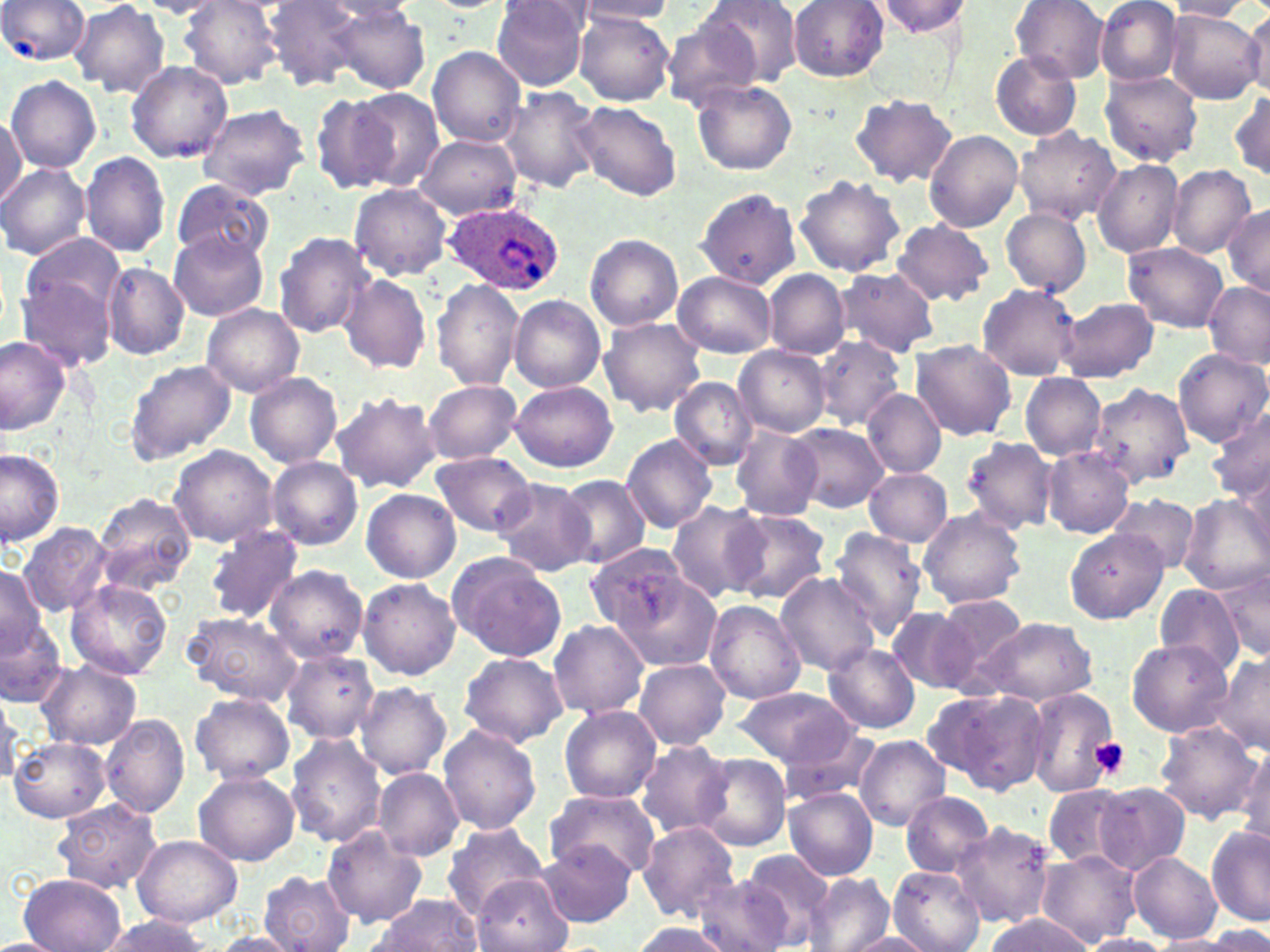

slide-level diagnosis = Plasmodium ovale
field of view = one of a larger specimen
uninfected red blood cell locations = approximate bounding boxes as named x1/y1/x2/y2 corners in pixels: (x1=0, y1=0, x2=90, y2=65), (x1=263, y1=0, x2=366, y2=89), (x1=577, y1=0, x2=679, y2=24), (x1=697, y1=0, x2=803, y2=88), (x1=1010, y1=0, x2=1110, y2=83), (x1=1095, y1=0, x2=1181, y2=85), (x1=69, y1=1, x2=169, y2=96), (x1=134, y1=1, x2=227, y2=17), (x1=178, y1=1, x2=286, y2=88), (x1=490, y1=1, x2=591, y2=90), (x1=788, y1=1, x2=889, y2=81), (x1=875, y1=1, x2=973, y2=38), (x1=1164, y1=1, x2=1252, y2=21), (x1=320, y1=2, x2=417, y2=23), (x1=331, y1=6, x2=431, y2=93), (x1=1165, y1=10, x2=1264, y2=105), (x1=1243, y1=10, x2=1270, y2=98), (x1=574, y1=11, x2=674, y2=106), (x1=660, y1=17, x2=762, y2=111), (x1=425, y1=46, x2=529, y2=147), (x1=991, y1=51, x2=1082, y2=140), (x1=126, y1=61, x2=233, y2=162), (x1=1100, y1=69, x2=1203, y2=166), (x1=6, y1=75, x2=101, y2=173), (x1=691, y1=80, x2=797, y2=177), (x1=498, y1=86, x2=604, y2=194), (x1=349, y1=88, x2=445, y2=191), (x1=1229, y1=89, x2=1270, y2=183), (x1=310, y1=93, x2=398, y2=195), (x1=851, y1=93, x2=957, y2=188), (x1=573, y1=101, x2=682, y2=199), (x1=195, y1=102, x2=310, y2=200), (x1=0, y1=116, x2=24, y2=206), (x1=1014, y1=127, x2=1120, y2=224), (x1=924, y1=129, x2=1024, y2=232), (x1=415, y1=134, x2=520, y2=220), (x1=79, y1=151, x2=171, y2=257), (x1=1092, y1=160, x2=1182, y2=258), (x1=0, y1=163, x2=91, y2=261), (x1=1166, y1=165, x2=1256, y2=258), (x1=794, y1=173, x2=906, y2=277), (x1=170, y1=179, x2=275, y2=265), (x1=350, y1=184, x2=453, y2=280), (x1=694, y1=187, x2=801, y2=289), (x1=1223, y1=205, x2=1270, y2=297), (x1=1001, y1=208, x2=1091, y2=297), (x1=893, y1=220, x2=994, y2=304), (x1=169, y1=231, x2=268, y2=321), (x1=274, y1=232, x2=375, y2=339), (x1=20, y1=233, x2=125, y2=323), (x1=585, y1=234, x2=683, y2=332), (x1=1124, y1=242, x2=1229, y2=333), (x1=101, y1=263, x2=190, y2=358), (x1=835, y1=267, x2=939, y2=356), (x1=104, y1=268, x2=201, y2=442), (x1=763, y1=270, x2=849, y2=357), (x1=673, y1=271, x2=778, y2=357), (x1=16, y1=272, x2=118, y2=371), (x1=338, y1=274, x2=432, y2=374), (x1=432, y1=278, x2=526, y2=392), (x1=1202, y1=281, x2=1269, y2=370), (x1=977, y1=284, x2=1083, y2=380), (x1=509, y1=295, x2=606, y2=392), (x1=1060, y1=297, x2=1158, y2=383), (x1=200, y1=303, x2=305, y2=397), (x1=598, y1=317, x2=706, y2=417), (x1=812, y1=335, x2=906, y2=430), (x1=0, y1=336, x2=71, y2=435), (x1=910, y1=340, x2=1016, y2=439), (x1=734, y1=346, x2=831, y2=436), (x1=1173, y1=349, x2=1269, y2=447), (x1=124, y1=359, x2=236, y2=464), (x1=245, y1=372, x2=341, y2=467), (x1=1020, y1=374, x2=1106, y2=460), (x1=669, y1=376, x2=758, y2=469), (x1=424, y1=379, x2=524, y2=464), (x1=509, y1=379, x2=620, y2=471), (x1=1086, y1=381, x2=1193, y2=490), (x1=862, y1=387, x2=946, y2=478), (x1=331, y1=392, x2=441, y2=495), (x1=635, y1=400, x2=755, y2=518), (x1=1209, y1=409, x2=1270, y2=503), (x1=787, y1=421, x2=889, y2=512), (x1=730, y1=425, x2=824, y2=521), (x1=620, y1=433, x2=720, y2=534), (x1=959, y1=435, x2=1057, y2=534), (x1=168, y1=445, x2=277, y2=548), (x1=1042, y1=446, x2=1134, y2=538), (x1=0, y1=448, x2=65, y2=548), (x1=431, y1=452, x2=536, y2=537), (x1=267, y1=456, x2=363, y2=551), (x1=863, y1=468, x2=953, y2=547), (x1=1239, y1=471, x2=1270, y2=561), (x1=557, y1=474, x2=650, y2=569), (x1=492, y1=476, x2=596, y2=578), (x1=361, y1=489, x2=460, y2=582), (x1=92, y1=493, x2=196, y2=595), (x1=1110, y1=494, x2=1199, y2=573), (x1=1179, y1=494, x2=1269, y2=594), (x1=665, y1=501, x2=768, y2=603), (x1=726, y1=509, x2=829, y2=605), (x1=918, y1=509, x2=1026, y2=609), (x1=18, y1=521, x2=114, y2=617), (x1=204, y1=526, x2=305, y2=624), (x1=828, y1=528, x2=928, y2=638), (x1=1064, y1=528, x2=1168, y2=625), (x1=585, y1=543, x2=696, y2=635), (x1=445, y1=552, x2=569, y2=661), (x1=264, y1=565, x2=369, y2=663), (x1=1218, y1=566, x2=1269, y2=664), (x1=0, y1=567, x2=45, y2=661), (x1=604, y1=570, x2=722, y2=673), (x1=774, y1=572, x2=880, y2=675), (x1=358, y1=577, x2=460, y2=680), (x1=65, y1=578, x2=173, y2=680), (x1=1156, y1=587, x2=1243, y2=668), (x1=933, y1=594, x2=1028, y2=685), (x1=705, y1=601, x2=805, y2=706), (x1=888, y1=607, x2=977, y2=694), (x1=183, y1=610, x2=305, y2=705), (x1=975, y1=617, x2=1096, y2=707), (x1=549, y1=618, x2=649, y2=719), (x1=0, y1=622, x2=69, y2=710), (x1=1127, y1=639, x2=1232, y2=738), (x1=822, y1=643, x2=919, y2=733), (x1=279, y1=649, x2=380, y2=743), (x1=458, y1=652, x2=568, y2=748), (x1=1212, y1=653, x2=1270, y2=754), (x1=38, y1=659, x2=142, y2=750), (x1=633, y1=659, x2=731, y2=750), (x1=354, y1=682, x2=451, y2=780), (x1=732, y1=686, x2=857, y2=768), (x1=924, y1=686, x2=1052, y2=797), (x1=1022, y1=687, x2=1122, y2=797), (x1=0, y1=693, x2=25, y2=784), (x1=191, y1=693, x2=295, y2=785), (x1=559, y1=706, x2=661, y2=804), (x1=101, y1=713, x2=190, y2=819), (x1=1150, y1=721, x2=1262, y2=822), (x1=438, y1=725, x2=541, y2=836), (x1=782, y1=725, x2=882, y2=807), (x1=285, y1=733, x2=386, y2=847), (x1=855, y1=735, x2=950, y2=830), (x1=9, y1=736, x2=111, y2=824), (x1=636, y1=740, x2=732, y2=839), (x1=1236, y1=742, x2=1270, y2=848), (x1=697, y1=754, x2=791, y2=851), (x1=374, y1=768, x2=464, y2=861), (x1=193, y1=771, x2=300, y2=866), (x1=1095, y1=782, x2=1192, y2=874), (x1=1040, y1=784, x2=1143, y2=870), (x1=785, y1=788, x2=878, y2=879), (x1=543, y1=789, x2=660, y2=881), (x1=901, y1=791, x2=993, y2=877), (x1=53, y1=799, x2=162, y2=893), (x1=950, y1=818, x2=1059, y2=930), (x1=639, y1=822, x2=739, y2=925), (x1=441, y1=823, x2=549, y2=920), (x1=1206, y1=825, x2=1270, y2=927), (x1=322, y1=826, x2=426, y2=928), (x1=131, y1=834, x2=242, y2=928), (x1=537, y1=842, x2=636, y2=928), (x1=742, y1=849, x2=834, y2=945), (x1=1128, y1=850, x2=1224, y2=943), (x1=1036, y1=851, x2=1140, y2=946), (x1=890, y1=865, x2=985, y2=952), (x1=259, y1=870, x2=356, y2=952), (x1=16, y1=873, x2=127, y2=952), (x1=471, y1=873, x2=571, y2=952), (x1=691, y1=873, x2=799, y2=952), (x1=805, y1=873, x2=892, y2=952), (x1=370, y1=894, x2=484, y2=952), (x1=988, y1=913, x2=1090, y2=952), (x1=97, y1=915, x2=213, y2=951), (x1=628, y1=922, x2=732, y2=951), (x1=204, y1=932, x2=305, y2=951), (x1=842, y1=932, x2=937, y2=951), (x1=0, y1=935, x2=61, y2=952), (x1=1079, y1=935, x2=1174, y2=952), (x1=1148, y1=936, x2=1243, y2=952)
modality = light microscopy
preparation = thin blood smear
stain = May-Grünwald-Giemsa
Plasmodium ovale-infected red blood cell locations = approximate bounding boxes as named x1/y1/x2/y2 corners in pixels: (x1=442, y1=201, x2=562, y2=293)
image size = 1270×952 pixels
magnification = 1000x
platelet locations = approximate bounding boxes as named x1/y1/x2/y2 corners in pixels: (x1=1087, y1=737, x2=1130, y2=780)